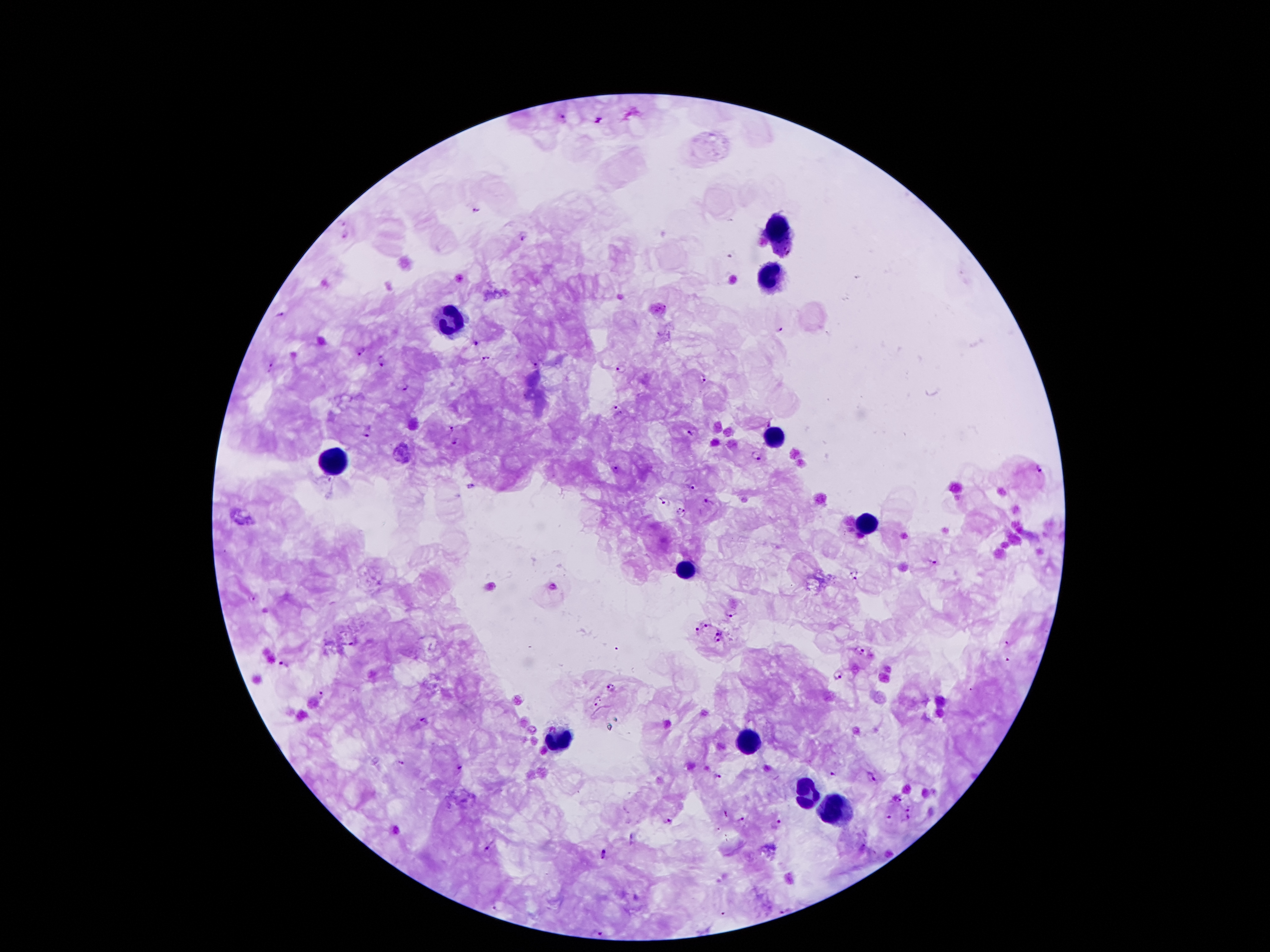 Approximate centers as [x, y] in pixels. Plasmodium parasite locations: [563, 119], [476, 211], [342, 223], [346, 236], [524, 239], [280, 312], [779, 328], [476, 344], [360, 350], [487, 358], [382, 361], [540, 365], [620, 368], [271, 369], [703, 378], [403, 385], [615, 407], [451, 429], [369, 432], [688, 434], [455, 442], [755, 455], [1039, 469], [616, 470], [690, 486], [471, 487], [667, 503], [709, 503], [680, 514], [932, 561], [855, 575], [553, 586], [254, 599], [731, 614], [706, 625], [697, 631], [718, 631], [720, 640], [1007, 642], [861, 652], [282, 662], [839, 674], [611, 689], [323, 693], [598, 700], [423, 720], [401, 762], [460, 767], [833, 773], [719, 776], [872, 777], [897, 799], [909, 807], [889, 817], [906, 817], [669, 820], [742, 820], [778, 824], [489, 848], [605, 854], [494, 907], [785, 910], [601, 932]. Leukocyte locations: [779, 232], [769, 275], [449, 318], [771, 435], [336, 462], [865, 521], [685, 570], [558, 736], [744, 740], [801, 791], [834, 806]. Smartphone photograph taken through the microscope eyepiece. Patient malaria status: infected with Plasmodium falciparum. Giemsa-stained preparation. Thick blood smear. One field from this slide. 100x magnification. Image is 1270×952 pixels.